Identify the blood parasite species.
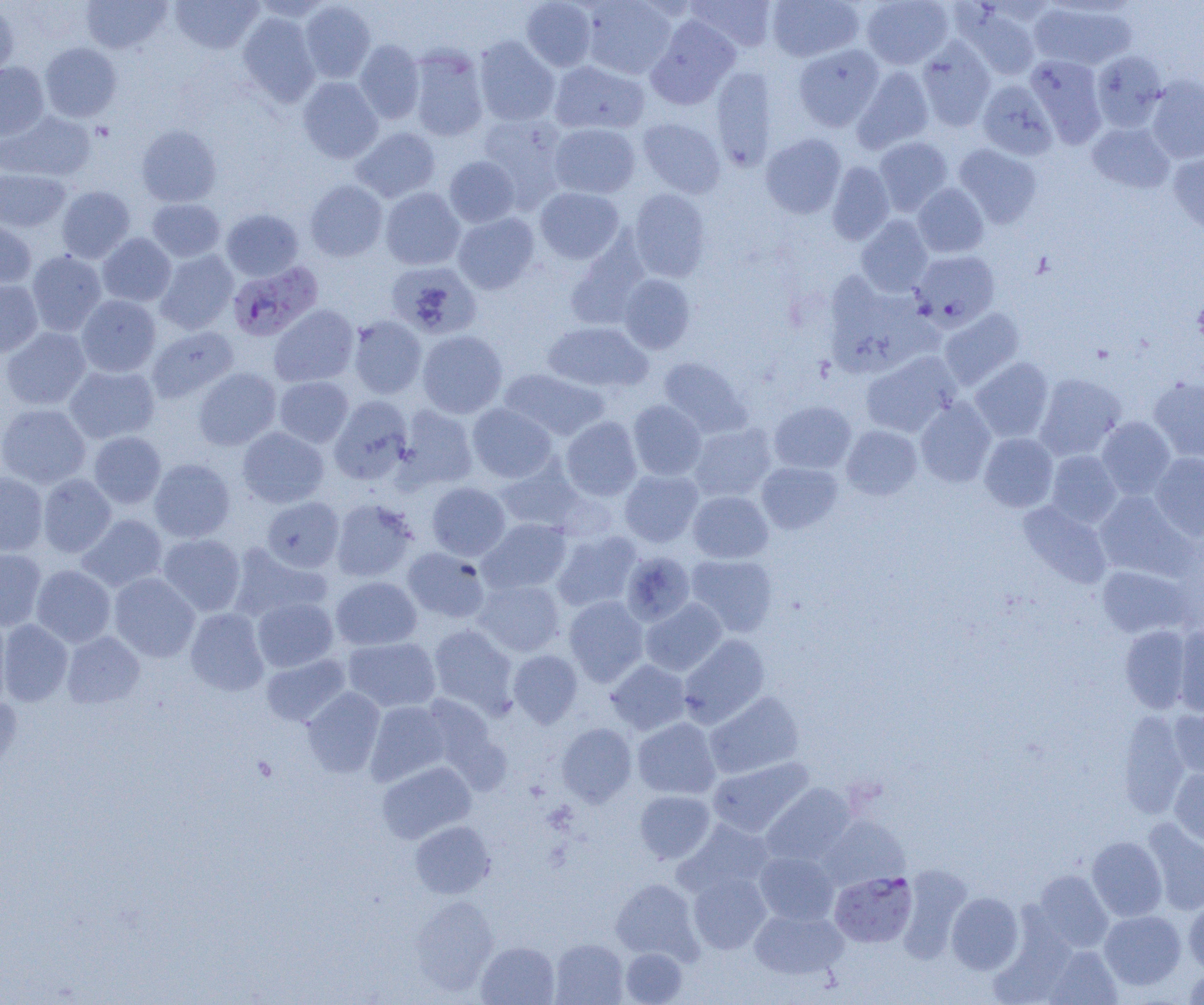
Plasmodium falciparum.

preparation: thin blood film
field_of_view: one of a larger specimen
magnification: 1000x
modality: light microscopy
image_size: 1204×1005 pixels
plasmodium_falciparum_infected_red_blood_cell_locations: 'approximate bounding boxes as (x1,y1)-(x2,y2) corner pairs in pixels: (227,260)-(323,341), (830,871)-(918,948)'
uninfected_red_blood_cell_locations: 'approximate bounding boxes as (x1,y1)-(x2,y2) corner pairs in pixels: (81,0)-(171,54), (170,0)-(262,54), (251,0)-(333,22), (521,0)-(596,71), (581,0)-(678,79), (686,0)-(777,52), (766,0)-(863,62), (861,0)-(953,69), (299,1)-(376,83), (1030,2)-(1138,70), (0,3)-(18,79), (955,4)-(1042,81), (238,12)-(321,106), (646,15)-(741,108), (474,37)-(559,126), (916,38)-(996,131), (354,40)-(425,124), (40,43)-(121,122), (793,44)-(885,131), (407,47)-(489,141), (1091,50)-(1167,131), (1025,55)-(1107,145), (549,60)-(649,135), (0,61)-(49,140), (852,65)-(935,153), (710,67)-(777,170), (1145,75)-(1204,163), (297,77)-(383,163), (977,79)-(1057,160), (1,111)-(96,182), (476,114)-(568,203), (637,117)-(725,198), (1087,122)-(1175,193), (549,123)-(640,198), (136,125)-(221,207), (350,127)-(441,203), (760,134)-(847,218), (874,136)-(953,216), (953,143)-(1042,228), (1168,150)-(1204,237), (444,156)-(520,227), (827,161)-(894,245), (0,168)-(70,232), (305,180)-(388,262), (913,183)-(988,258), (56,186)-(135,263), (380,187)-(465,270), (535,187)-(624,263), (628,189)-(711,281), (146,198)-(225,262), (222,209)-(304,281), (452,212)-(540,294), (856,215)-(933,296), (0,220)-(36,289), (97,233)-(176,307), (565,236)-(649,331), (27,250)-(107,336), (155,250)-(238,335), (910,251)-(999,329), (386,261)-(482,338), (619,274)-(696,353), (824,274)-(934,376), (0,280)-(43,356), (76,295)-(161,377), (269,304)-(359,387), (938,308)-(1024,390), (348,315)-(427,399), (542,321)-(652,393), (146,326)-(239,404), (1,327)-(91,410), (417,330)-(507,418), (861,350)-(961,437), (658,357)-(751,437), (970,357)-(1054,442), (64,364)-(160,444), (193,368)-(281,450), (499,368)-(609,441), (1034,373)-(1126,460), (274,376)-(354,447), (1148,376)-(1204,462), (329,396)-(413,484), (915,397)-(996,488), (628,400)-(706,480), (769,400)-(856,474), (0,403)-(91,489), (467,403)-(557,483), (396,406)-(478,490), (1096,416)-(1176,498), (561,417)-(642,500), (688,423)-(776,502), (841,424)-(922,499), (237,426)-(329,508), (88,431)-(166,508), (979,433)-(1058,512), (1046,450)-(1121,528), (1149,452)-(1204,539), (496,457)-(585,533), (149,458)-(235,543), (756,461)-(843,534), (620,469)-(703,547), (0,471)-(48,556), (37,474)-(116,557), (427,482)-(511,560), (688,490)-(773,563), (1094,491)-(1194,580), (262,496)-(344,572), (331,498)-(418,582), (1018,500)-(1112,588), (77,514)-(168,593), (478,518)-(572,594), (552,530)-(642,612), (157,534)-(245,616), (228,543)-(330,623), (402,547)-(491,623), (0,548)-(47,631), (621,551)-(695,626), (686,554)-(778,637), (31,565)-(115,647), (1097,565)-(1194,639), (109,572)-(200,662), (331,576)-(422,650), (473,579)-(564,656), (252,596)-(338,672), (564,596)-(648,685), (640,599)-(727,676), (185,608)-(269,695), (0,614)-(11,708), (0,619)-(73,706), (429,624)-(519,716), (1120,625)-(1192,713), (1173,626)-(1204,716), (62,632)-(145,709), (678,634)-(770,727), (343,637)-(441,712), (508,650)-(582,727), (261,653)-(350,726), (606,659)-(690,734), (301,687)-(384,777), (704,691)-(804,780), (0,697)-(22,781), (365,701)-(451,785), (1169,707)-(1204,780), (1117,712)-(1190,819), (632,717)-(721,799), (557,723)-(637,806), (707,757)-(813,837), (377,761)-(476,844), (1169,768)-(1204,847), (761,783)-(857,867), (635,790)-(715,863), (818,814)-(910,889), (676,819)-(775,898), (1142,819)-(1204,915), (410,820)-(495,898), (1087,836)-(1167,921), (754,851)-(840,925), (904,866)-(976,964), (1033,870)-(1113,952), (688,872)-(771,954), (610,878)-(701,962), (946,892)-(1024,974), (1184,896)-(1204,975), (411,897)-(498,994), (749,908)-(849,981), (1099,910)-(1186,990), (550,938)-(628,1005), (476,941)-(560,1005), (1043,945)-(1122,1005), (620,948)-(687,1004), (1183,967)-(1204,1004)'